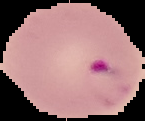

preparation = thin blood film
image type = segmented cell region on a black background
result = Plasmodium parasites identified
image size = 145×121 pixels